Assess this cell for malaria.
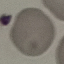
Uninfected.

Summary:
  - Preparation: thin smear
  - Stain: Giemsa
  - Image type: cell patch, automatically extracted from a larger field of view and resized to 64 × 64 pixels
  - Capture: smartphone through the microscope eyepiece